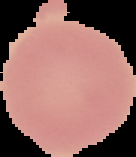
image_type: cell region segmented out of the field of view; surrounding area masked to black
result: no Plasmodium parasites detected
preparation: thin blood film
image_size: 136×157 pixels